Report the malaria status of this cell.
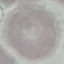

It is uninfected.

{
  "preparation": "thin blood smear",
  "image_type": "automatically extracted cell patch, resized to 64 × 64 pixels",
  "stain": "Giemsa",
  "capture": "smartphone through the microscope eyepiece"
}